Name the parasite shown.
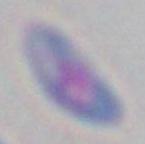
This is Toxoplasma gondii.

magnification = 1000x
modality = micrograph